Identify the parasite.
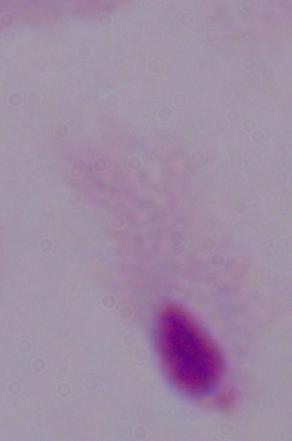

This is a trichomonad.

magnification = 1000x
modality = micrograph